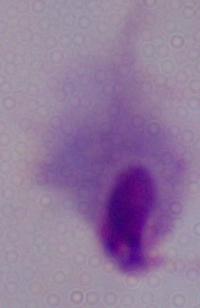
magnification = 1000x
modality = micrograph
identification = trichomonad